Name the cell type shown.
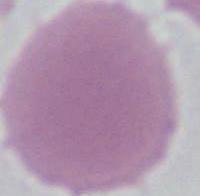
This is an erythrocyte.

Micrograph. Captured at 1000x magnification.